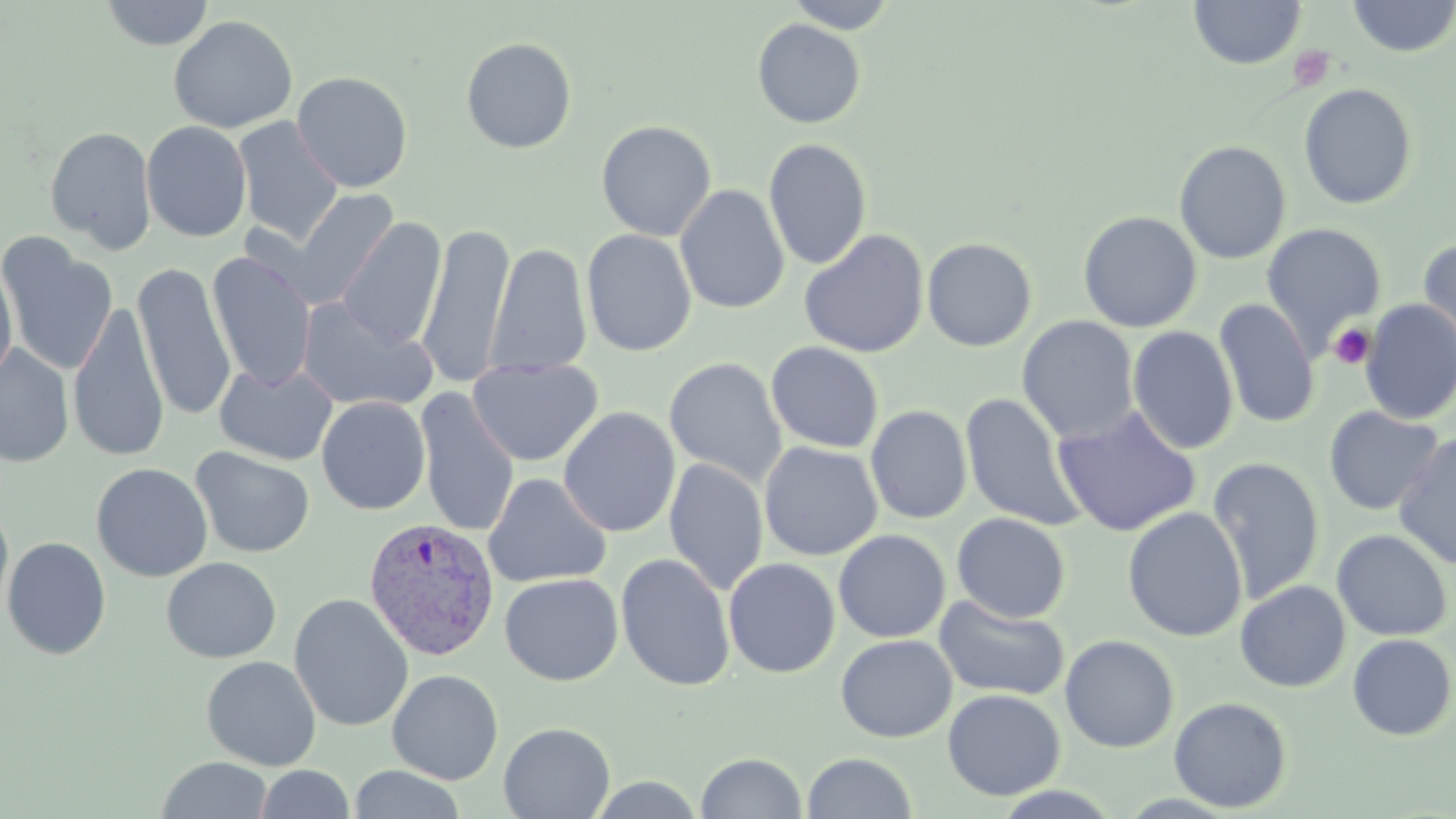
slide-level diagnosis = Plasmodium vivax
magnification = 1000x
platelet locations = approximate bounding boxes as [x1, y1, x2, y2] in pixels: [1288, 46, 1335, 93], [1328, 322, 1375, 370]
modality = light microscopy
Plasmodium vivax-infected red blood cell locations = approximate bounding boxes as [x1, y1, x2, y2] in pixels: [362, 517, 500, 661]
preparation = thin blood smear
stain = May-Grünwald-Giemsa
field of view = single
image size = 1456×819 pixels
uninfected red blood cell locations = approximate bounding boxes as [x1, y1, x2, y2] in pixels: [100, 0, 215, 50], [785, 0, 899, 33], [1189, 0, 1305, 69], [1346, 0, 1456, 58], [168, 15, 298, 134], [752, 19, 865, 129], [461, 37, 577, 154], [292, 71, 413, 192], [1299, 83, 1418, 210], [233, 117, 344, 247], [596, 120, 717, 242], [141, 121, 252, 242], [43, 125, 157, 254], [763, 138, 872, 270], [1174, 140, 1291, 264], [675, 184, 790, 315], [283, 188, 400, 309], [1078, 211, 1202, 333], [336, 218, 447, 350], [1261, 222, 1387, 352], [417, 224, 514, 389], [581, 229, 697, 357], [798, 229, 929, 359], [0, 234, 117, 377], [922, 237, 1037, 352], [1417, 237, 1456, 369], [485, 243, 592, 378], [206, 252, 317, 391], [0, 259, 18, 386], [131, 263, 237, 421], [296, 296, 438, 413], [1214, 298, 1319, 429], [1359, 299, 1456, 425], [69, 300, 168, 462], [1017, 316, 1139, 443], [1127, 325, 1239, 455], [765, 342, 884, 454], [0, 345, 74, 467], [665, 357, 787, 487], [468, 358, 603, 466], [214, 361, 338, 466], [415, 390, 520, 538], [959, 392, 1086, 532], [316, 396, 431, 516], [866, 405, 972, 524], [1052, 406, 1201, 537], [1324, 406, 1445, 516], [558, 407, 681, 538], [1393, 432, 1456, 570], [759, 442, 883, 560], [190, 446, 315, 559], [1207, 457, 1325, 604], [665, 458, 769, 596], [91, 463, 212, 582], [483, 473, 612, 589], [0, 505, 15, 625], [1122, 506, 1248, 643], [951, 513, 1071, 623], [833, 529, 950, 643], [1331, 529, 1453, 641], [2, 535, 112, 660], [615, 552, 736, 692], [161, 557, 281, 663], [722, 558, 840, 678], [499, 573, 623, 686], [1235, 580, 1351, 692], [289, 592, 414, 732], [934, 594, 1069, 702], [1347, 633, 1455, 740], [836, 634, 957, 742], [1060, 634, 1179, 752], [201, 655, 321, 770], [387, 669, 503, 785], [942, 688, 1066, 801], [1169, 696, 1292, 812], [499, 721, 615, 818], [695, 752, 807, 818], [801, 752, 919, 818], [155, 757, 273, 818], [255, 765, 354, 819], [348, 765, 467, 819]